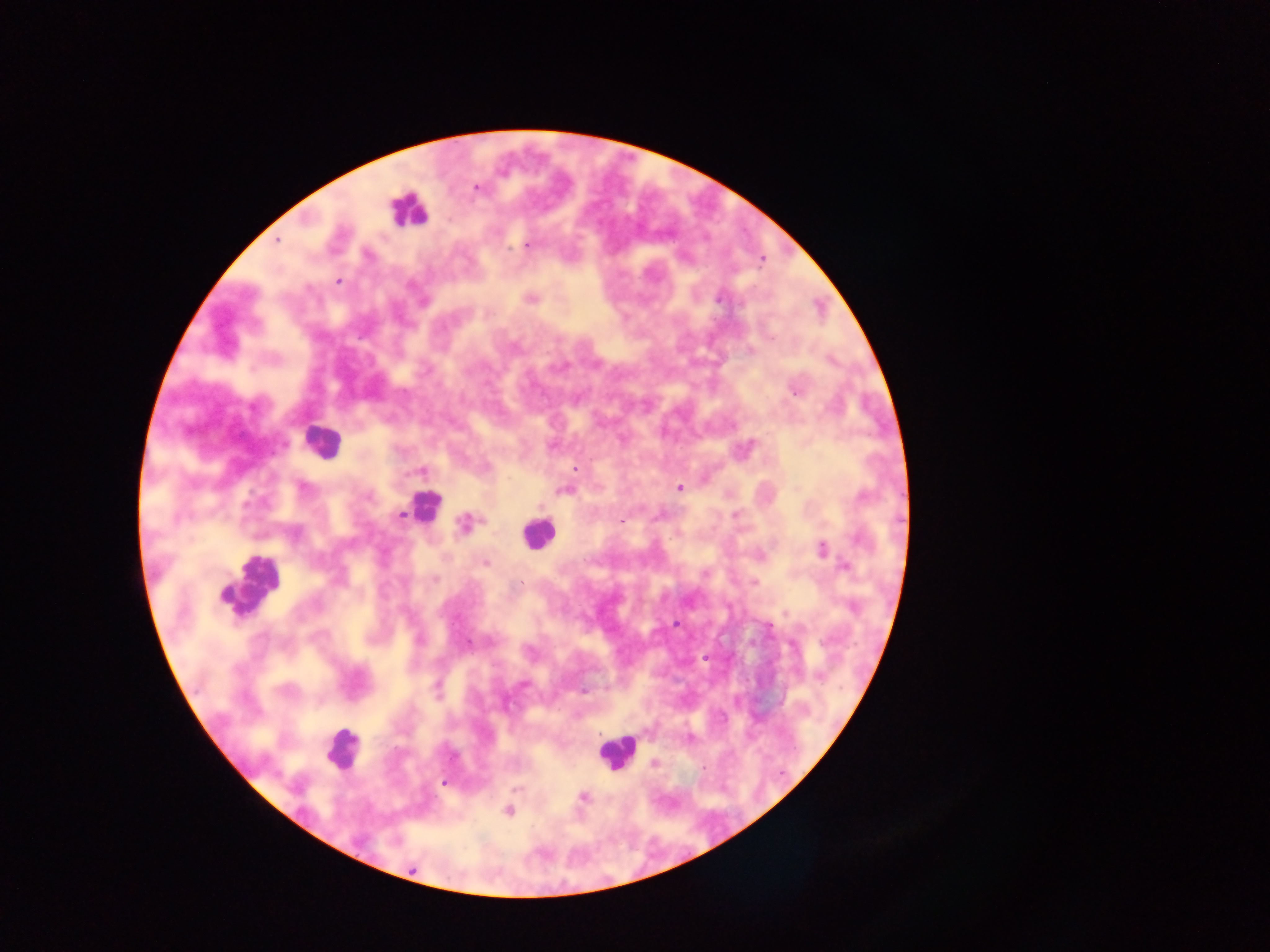
leukocyte_locations: 'approximate centers as x y in pixels: 408 210; 321 442; 423 506; 537 533; 249 586; 341 749; 615 752'
capture: mobile-phone photograph through a microscope
country: Ghana
malaria_parasite_locations: 'approximate centers as x y in pixels: 475 187; 277 239; 526 244; 762 259; 337 280; 720 296; 530 298; 423 301; 749 350; 795 390; 576 469; 421 471; 678 488; 797 489; 565 490; 401 516; 621 519; 465 524; 822 549; 485 562; 845 566; 754 582; 676 624; 468 643; 819 677; 524 684; 584 692; 688 739; 653 763; 444 782; 516 788; 583 796; 508 810'
field_of_view: single
image_size: 1270×952 pixels
preparation: thick blood smear